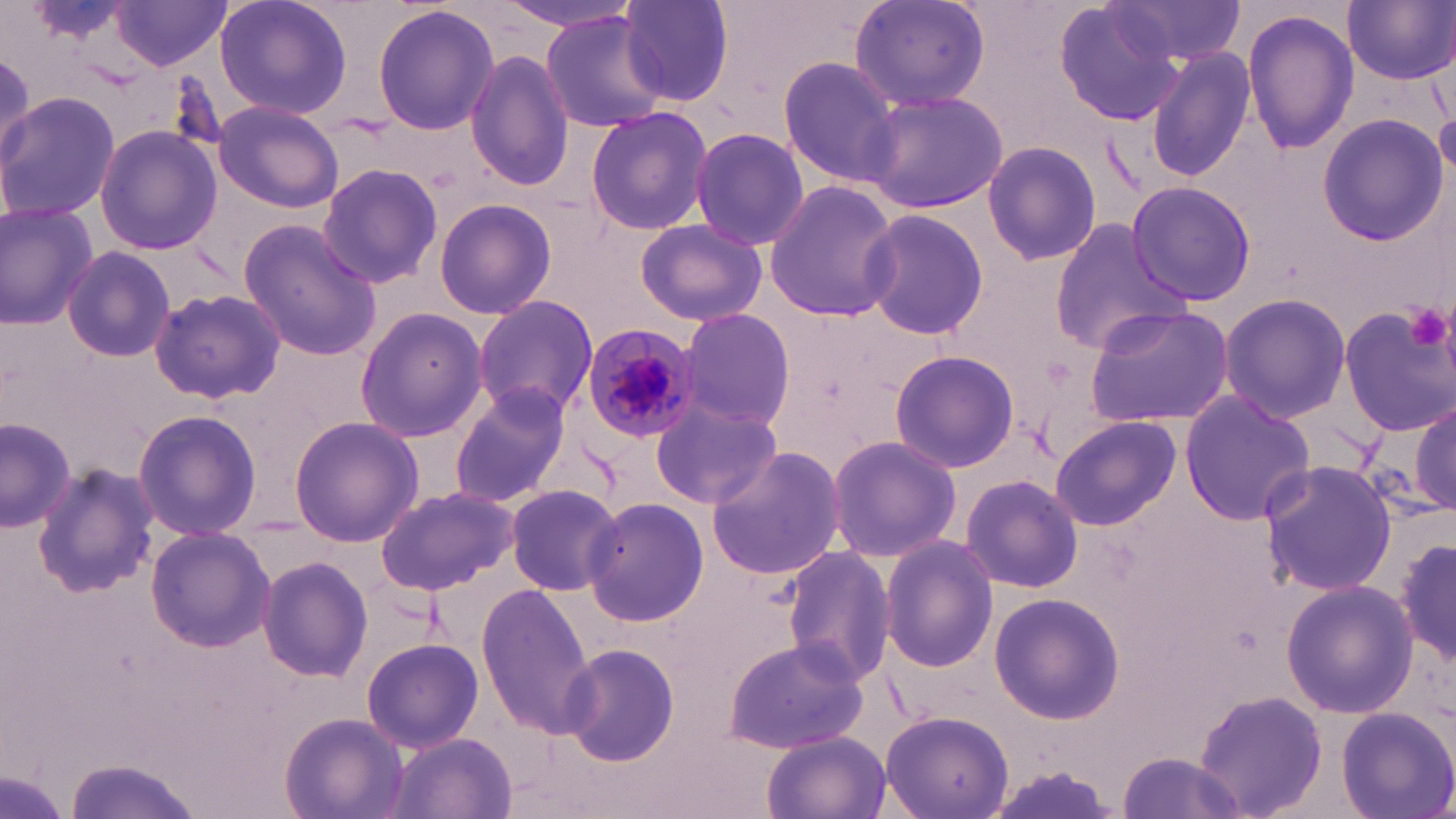

Summary:
  - Coordinate format: approximate bounding boxes as [x1, y1, x2, y2] in pixels
  - Platelet locations: [1403, 302, 1453, 351]
  - Uninfected red blood cell locations: [110, 0, 232, 70], [214, 0, 352, 121], [493, 0, 645, 33], [848, 0, 991, 113], [1110, 0, 1244, 72], [1344, 0, 1454, 84], [621, 1, 736, 107], [1053, 2, 1184, 127], [372, 3, 500, 136], [539, 9, 669, 134], [1243, 10, 1358, 156], [1144, 44, 1258, 187], [0, 49, 34, 172], [465, 49, 574, 191], [777, 56, 902, 187], [863, 90, 1008, 213], [0, 91, 120, 221], [213, 101, 344, 211], [585, 104, 713, 236], [1435, 109, 1455, 185], [1318, 115, 1447, 245], [95, 126, 223, 255], [690, 127, 809, 250], [982, 139, 1102, 267], [316, 163, 444, 290], [763, 179, 900, 322], [1127, 179, 1253, 307], [433, 198, 557, 319], [0, 202, 100, 328], [860, 208, 989, 340], [634, 218, 766, 325], [237, 219, 383, 362], [1048, 219, 1187, 354], [63, 246, 175, 364], [149, 287, 287, 405], [472, 294, 597, 421], [1220, 295, 1353, 423], [1082, 302, 1236, 427], [1342, 303, 1455, 435], [354, 308, 487, 444], [679, 308, 796, 430], [888, 349, 1020, 473], [449, 384, 575, 507], [1179, 391, 1317, 525], [650, 400, 781, 510], [1412, 401, 1455, 514], [131, 409, 263, 540], [1049, 415, 1180, 531], [0, 416, 77, 531], [288, 416, 423, 546], [826, 434, 961, 563], [705, 446, 848, 579], [1256, 459, 1398, 597], [32, 466, 158, 598], [961, 474, 1084, 593], [504, 483, 622, 596], [374, 486, 517, 595], [581, 495, 708, 629], [146, 526, 275, 653], [1394, 533, 1455, 668], [880, 535, 998, 674], [780, 544, 897, 690], [256, 556, 373, 683], [1280, 579, 1420, 719], [476, 586, 596, 736], [988, 593, 1126, 724], [721, 637, 871, 755], [361, 638, 482, 752], [557, 643, 679, 764], [1195, 692, 1328, 816], [1337, 705, 1455, 818], [280, 711, 407, 819], [879, 711, 1014, 819], [762, 731, 889, 819], [385, 732, 518, 818], [1118, 750, 1243, 817], [66, 754, 202, 819]
  - Plasmodium malariae-infected red blood cell locations: [581, 322, 703, 448]
  - Slide-level diagnosis: Plasmodium malariae
  - Image size: 1456×819 pixels
  - Modality: optical microscopy
  - Field of view: single
  - Preparation: thin blood film
  - Stain: May-Grünwald-Giemsa
  - Magnification: 1000x